Assess for malaria.
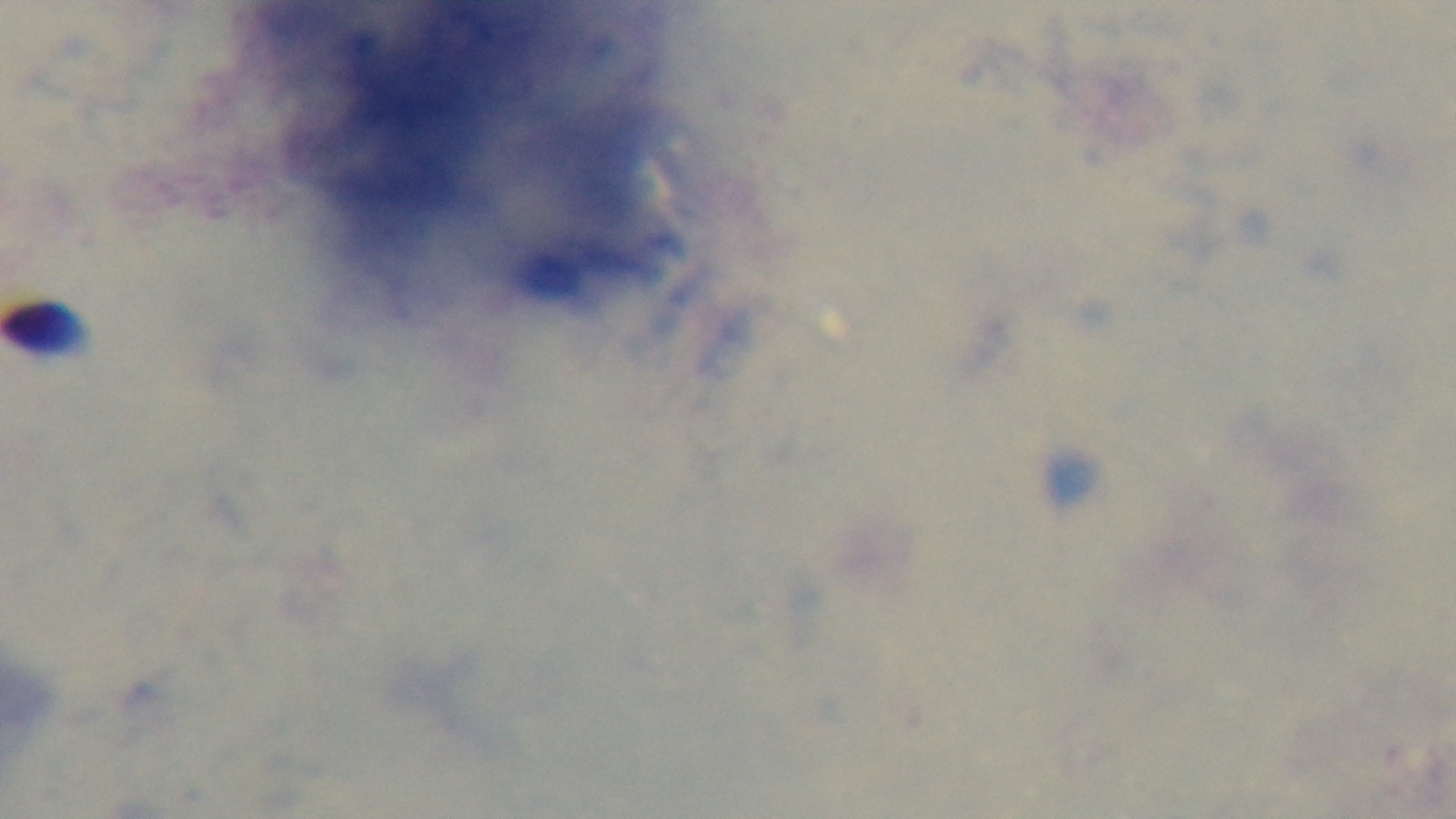

Negative.

Mounted 4K digital camera. Photomicrograph. Preparation: thick. Single field of view. Giemsa-stained. Oil-immersion objective, 100x.